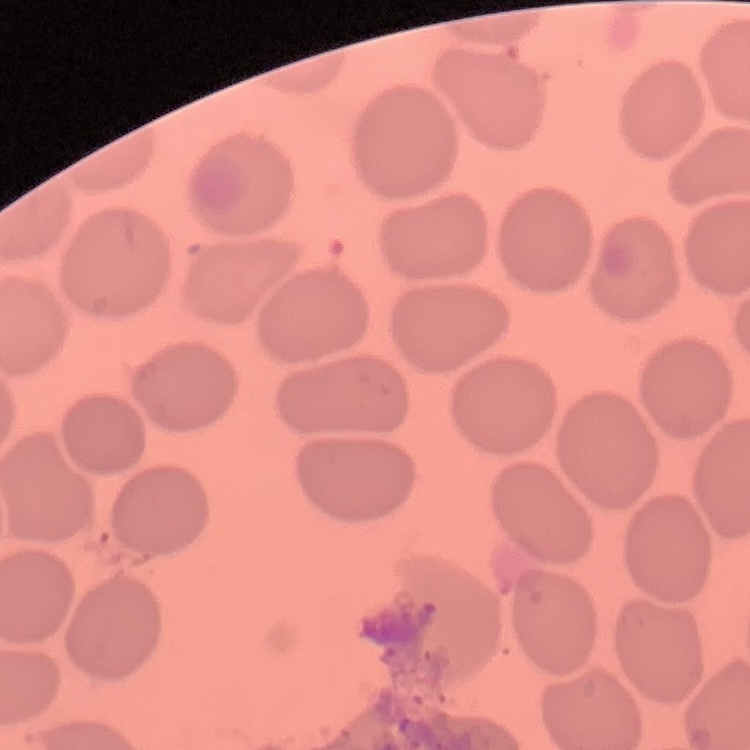
red blood cell morphology = no rouleaux formation
preparation = thin peripheral smear
image type = square crop of a larger photomicrograph
stain = Field's or Giemsa